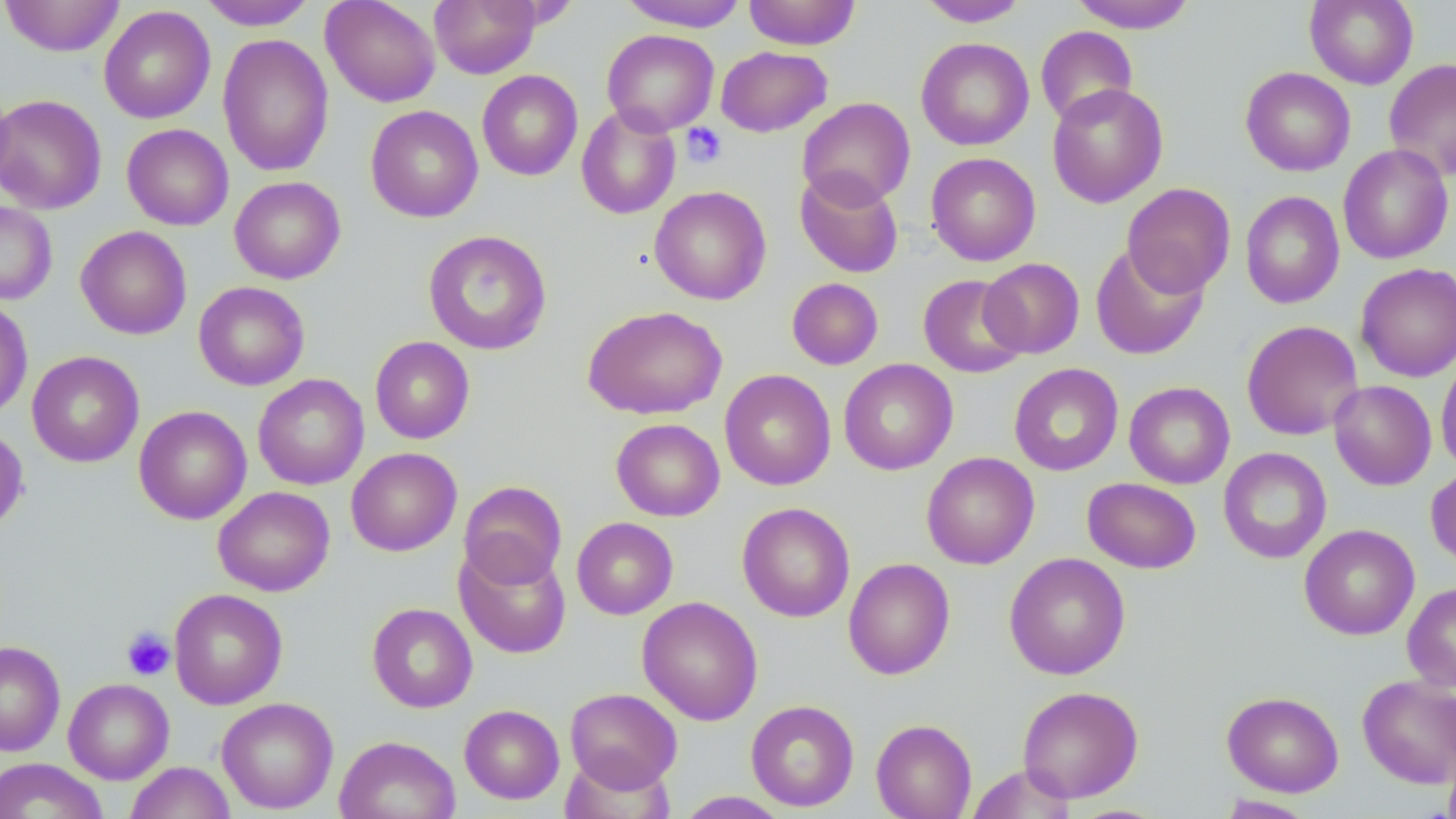 Approximate bounding boxes as (x1,y1)-(x2,y2) corner pairs in pixels. Platelet locations: (681,123)-(727,168), (121,627)-(175,681). Uninfected red blood cell locations: (1,0)-(125,57), (198,0)-(317,30), (321,0)-(441,107), (430,0)-(541,78), (743,0)-(861,50), (917,0)-(1030,27), (1068,0)-(1197,32), (1304,0)-(1419,89), (618,1)-(748,32), (98,5)-(216,124), (1035,26)-(1138,127), (601,29)-(719,135), (217,33)-(334,177), (916,37)-(1034,151), (716,46)-(832,137), (1383,59)-(1456,181), (1241,67)-(1355,176), (477,70)-(583,181), (1047,83)-(1168,207), (0,94)-(107,214), (798,97)-(916,208), (365,105)-(483,223), (576,106)-(681,219), (122,124)-(233,231), (1338,144)-(1453,264), (925,153)-(1040,266), (795,169)-(904,278), (229,176)-(345,284), (1122,183)-(1235,297), (649,186)-(772,305), (1240,191)-(1344,309), (0,201)-(57,305), (76,226)-(191,339), (423,230)-(552,355), (1089,243)-(1210,360), (979,257)-(1085,359), (1355,263)-(1455,381), (918,274)-(1029,378), (787,277)-(883,369), (193,281)-(310,390), (0,299)-(33,420), (583,305)-(727,420), (1241,320)-(1364,441), (370,336)-(475,444), (26,350)-(144,468), (1436,354)-(1456,475), (838,358)-(958,476), (1008,363)-(1124,476), (720,369)-(836,490), (253,373)-(369,490), (1329,380)-(1436,490), (1124,381)-(1234,488), (134,405)-(252,525), (611,418)-(724,521), (0,425)-(29,535), (346,447)-(462,556), (1218,447)-(1331,564), (921,451)-(1039,569), (1426,466)-(1456,570), (1082,477)-(1201,573), (458,480)-(567,588), (213,486)-(335,596), (737,502)-(855,622), (572,517)-(678,619), (1299,524)-(1420,640), (455,542)-(571,659), (1004,552)-(1131,680), (843,558)-(956,680), (1402,582)-(1456,692), (169,588)-(288,709), (637,596)-(763,725), (367,602)-(478,713), (0,641)-(65,757), (1358,675)-(1456,787), (63,678)-(174,784), (1017,685)-(1143,803), (564,687)-(682,791), (1222,691)-(1344,797), (216,697)-(338,814), (745,699)-(859,811), (459,704)-(564,804), (871,718)-(977,818), (334,735)-(460,819), (1443,748)-(1456,819), (0,758)-(108,819), (124,761)-(236,819), (965,764)-(1078,819), (675,791)-(790,818), (1216,795)-(1316,818). Slide-level diagnosis: no evidence of blood parasites. Captured at 1000x magnification. Single field of view. Image is 1456×819 pixels. Thin blood film. May-Grünwald-Giemsa stain. Optical microscopy.